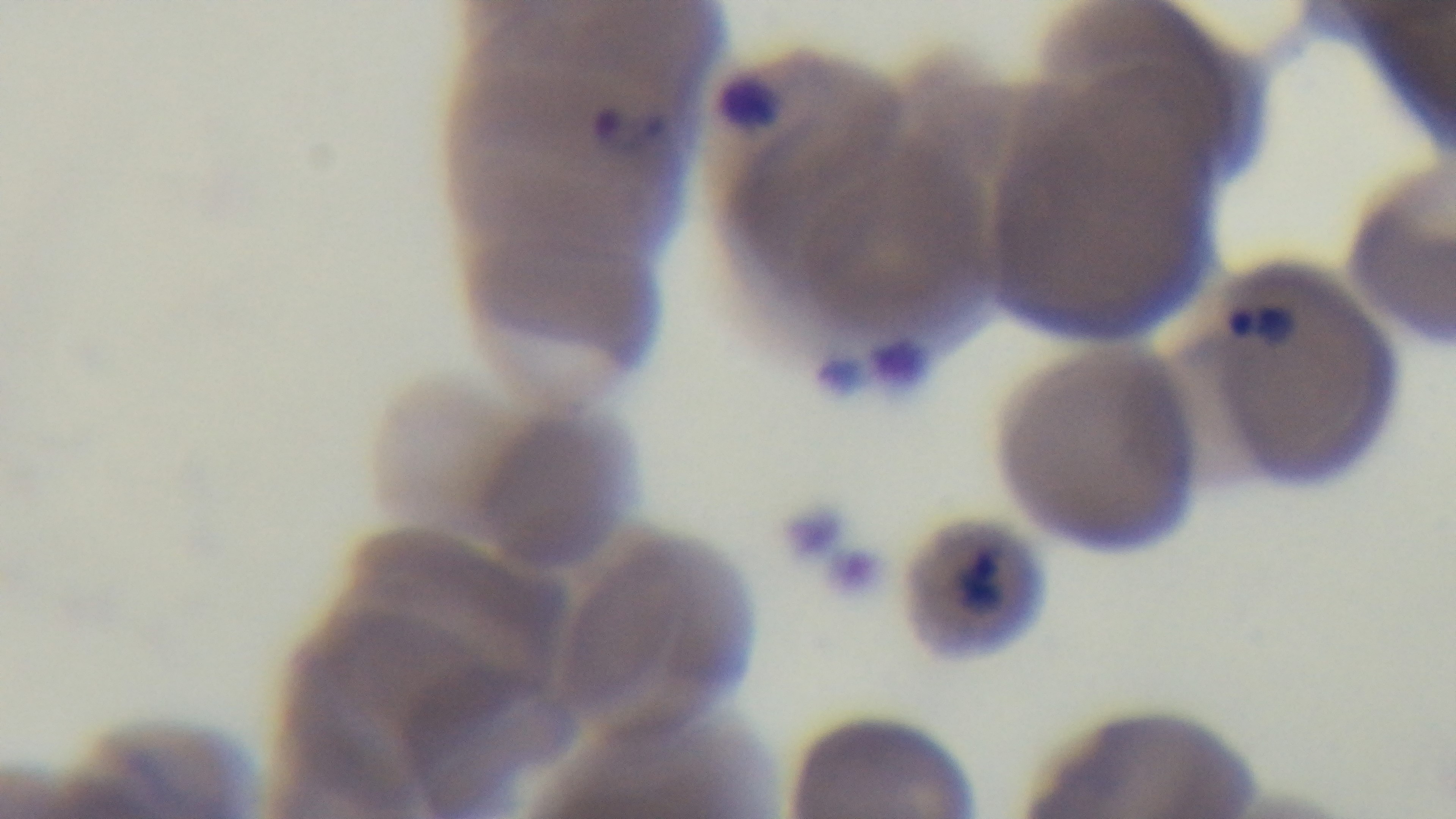

Summary:
  - Malaria status: positive
  - Objective: 100x oil immersion
  - Capture: mounted 4K digital camera
  - Modality: light microscopy
  - Field of view: one from the slide
  - Stain: Giemsa
  - Preparation: thin blood film